Point out every malaria parasite and every leukocyte.
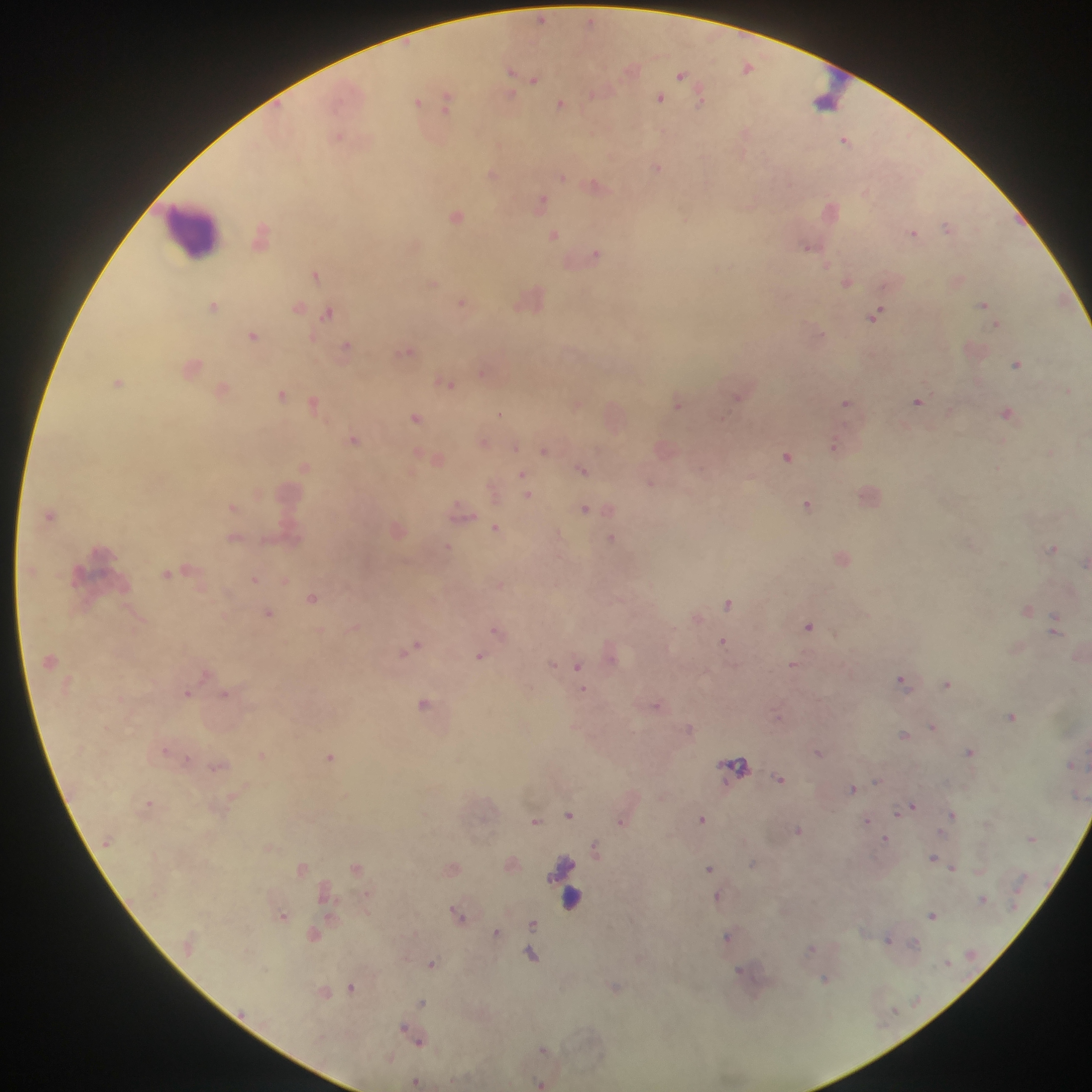

Approximate centers as x y in pixels.
Malaria parasites: 541 19; 590 20; 748 67; 631 69; 511 71; 681 74; 535 80; 594 93; 510 95; 660 98; 417 100; 701 100; 447 101; 560 104; 339 137; 845 139; 656 168; 492 174; 562 176; 596 184; 541 203; 457 216; 947 227; 913 233; 262 234; 554 235; 807 246; 596 255; 826 264; 315 275; 846 282; 433 283; 530 298; 463 303; 983 303; 213 305; 298 306; 328 312; 876 315; 996 324; 253 335; 346 346; 408 350; 1017 364; 483 372; 118 382; 449 384; 223 390; 281 394; 738 397; 918 401; 314 403; 845 403; 676 404; 578 405; 1007 412; 500 413; 416 418; 354 439; 483 442; 834 447; 515 448; 544 451; 1050 453; 786 456; 438 459; 305 467; 582 470; 523 476; 651 483; 527 494; 807 504; 232 507; 585 509; 461 512; 496 529; 235 538; 611 539; 448 548; 1052 549; 1085 563; 169 573; 254 579; 313 598; 729 603; 268 614; 1055 623; 808 625; 497 631; 723 642; 413 647; 479 656; 552 664; 792 664; 578 665; 902 680; 948 683; 583 689; 187 694; 225 694; 424 703; 657 705; 1011 716; 778 717; 933 727; 689 728; 903 734; 165 750; 969 752; 819 753; 262 755; 330 757; 736 765; 217 767; 779 779; 877 780; 852 789; 149 802; 910 807; 901 810; 569 815; 952 815; 702 818; 535 821; 622 821; 866 821; 798 830; 1032 838; 886 839; 595 848; 933 858; 753 864; 356 867; 953 867; 709 868; 302 869; 717 897; 983 899; 458 914; 933 915; 283 916; 532 924; 497 932; 314 935; 728 937; 888 938; 914 944; 811 949; 531 955; 947 962; 431 964; 825 979; 351 987; 615 987; 422 1003; 405 1031; 417 1039; 543 1050; 415 1081; 540 1083.
Leukocytes (some below the resolvable threshold): 841 80; 825 103; 192 231; 569 898.

Summary:
  - Preparation: thick blood film
  - Capture: mobile-phone photograph through a microscope
  - Country: Ghana
  - Image size: 1092×1092 pixels
  - Field of view: single